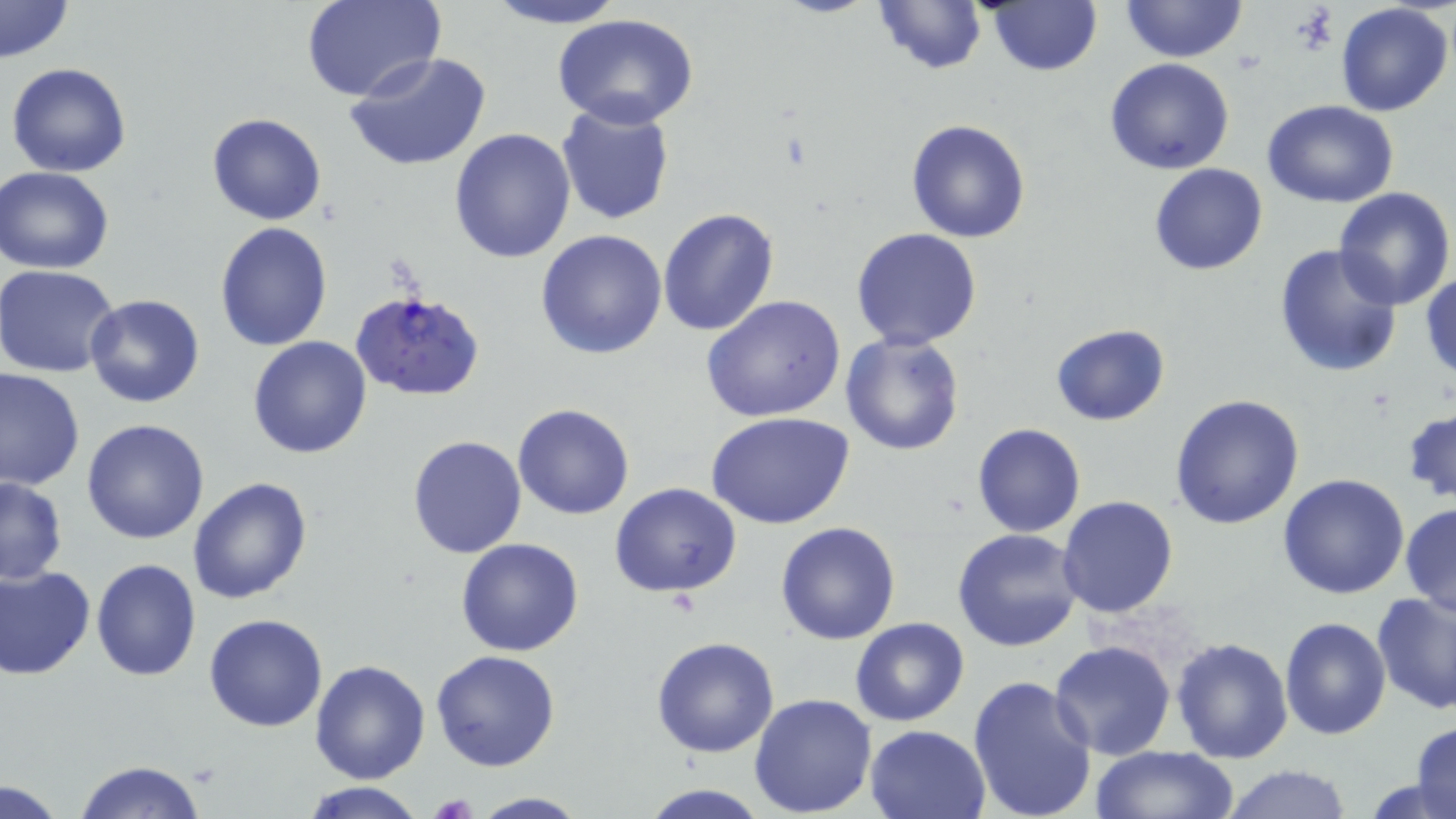 Approximate bounding boxes as (x1,y1)-(x2,y2) corner pairs in pixels. Platelet locations: (430,793)-(478,819). Uninfected red blood cell locations: (302,0)-(445,103), (477,0)-(627,29), (871,0)-(987,74), (1122,0)-(1247,62), (0,1)-(74,63), (984,3)-(1103,77), (1335,3)-(1453,117), (554,16)-(698,129), (343,53)-(493,173), (1104,57)-(1235,175), (6,62)-(132,178), (1262,99)-(1399,209), (554,102)-(674,226), (206,113)-(327,225), (906,118)-(1033,243), (449,128)-(577,264), (1149,163)-(1269,275), (1,166)-(118,273), (1333,189)-(1455,310), (657,208)-(778,337), (214,222)-(334,352), (850,227)-(983,349), (536,228)-(669,360), (1272,245)-(1402,378), (0,265)-(124,379), (1420,271)-(1455,384), (82,294)-(206,409), (702,295)-(847,424), (1050,322)-(1170,426), (839,333)-(967,457), (248,335)-(374,459), (0,368)-(84,492), (1169,393)-(1305,529), (513,403)-(635,520), (1404,408)-(1456,506), (709,413)-(854,531), (81,417)-(210,545), (972,422)-(1085,537), (407,434)-(528,558), (1277,473)-(1410,598), (0,476)-(68,586), (187,478)-(314,605), (610,483)-(742,599), (1058,495)-(1179,619), (1402,502)-(1456,619), (775,522)-(901,645), (952,527)-(1084,652), (456,538)-(584,657), (92,557)-(202,681), (0,564)-(95,680), (1372,592)-(1456,713), (204,612)-(328,732), (1279,616)-(1391,739), (850,618)-(970,728), (651,636)-(779,758), (1170,636)-(1293,763), (1048,640)-(1176,759), (431,649)-(562,772), (310,661)-(429,783), (967,674)-(1098,819), (749,693)-(877,816), (1409,722)-(1455,819), (865,724)-(990,819), (1089,745)-(1238,819), (74,760)-(208,819), (1220,764)-(1353,819), (0,780)-(69,819), (297,781)-(429,818), (638,784)-(770,818), (468,792)-(589,818). Plasmodium falciparum-infected red blood cell locations: (352,291)-(485,403). Slide-level diagnosis: Plasmodium falciparum. Captured at 1000x magnification. May-Grünwald-Giemsa-stained preparation. Single field of view. Optical microscopy. Image is 1456×819 pixels. Thin blood film.